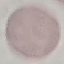
Result: no malaria parasites seen. Photographed with a smartphone camera at the microscope eyepiece. Thin blood smear. Automatically extracted cell patch, resized to 64 × 64 pixels. Giemsa stain.